Describe the morphology of the red blood cells.
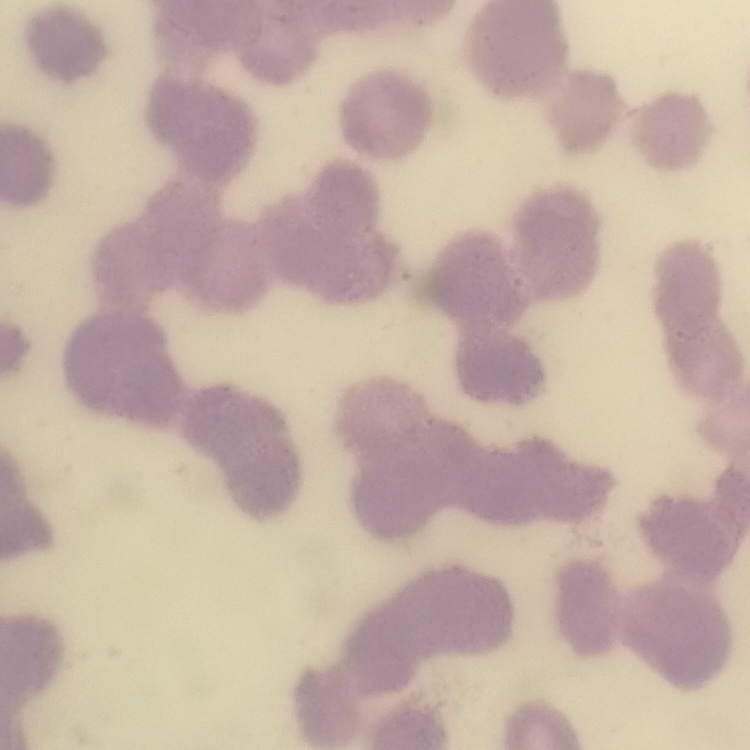

Rouleaux formation.

Summary:
  - Stain: Field's or Giemsa
  - Image type: square crop of a larger photomicrograph
  - Preparation: thin blood film